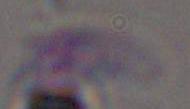

magnification = 1000x
identification = Toxoplasma gondii
modality = micrograph